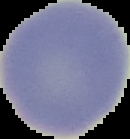
Summary:
  - Image size: 130×139 pixels
  - Result: no Plasmodium parasites detected
  - Preparation: thin blood film
  - Image type: cell region segmented out of the field of view; surrounding area masked to black